Identify the parasite.
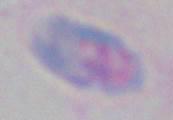
This is Toxoplasma gondii.

Summary:
  - Magnification: 1000x
  - Modality: micrograph